Report the malaria status of this cell.
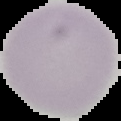
Uninfected.

Summary:
  - Image type: cell region segmented out of the field of view; surrounding area masked to black
  - Preparation: thin blood film
  - Image size: 121×121 pixels